Identify the preparation type.
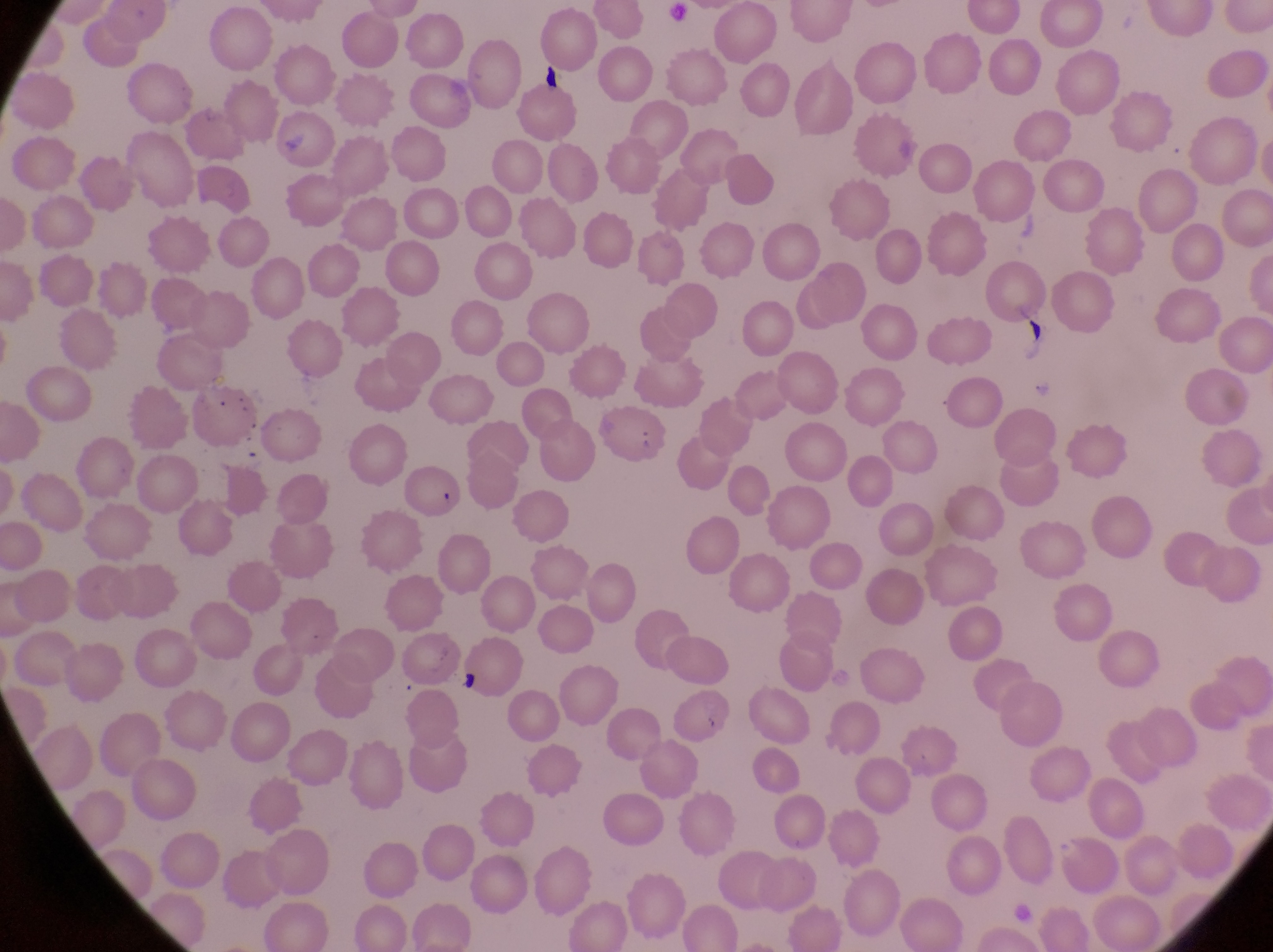
This is a thin smear.

Approximate bounding boxes as (left, top, right, bottom) in pixels. Artifact (platelet-like body, stain precipitate, or debris) locations: (277, 127, 309, 160). Trophozoite locations: (1029, 372, 1057, 404). Captured by a smartphone held over the eyepiece of an Olympus CX-23 microscope. Collected in Uganda. At a magnification of 1000x. Single field of view. Image is 1273×952 pixels.